Identify the blood parasite species.
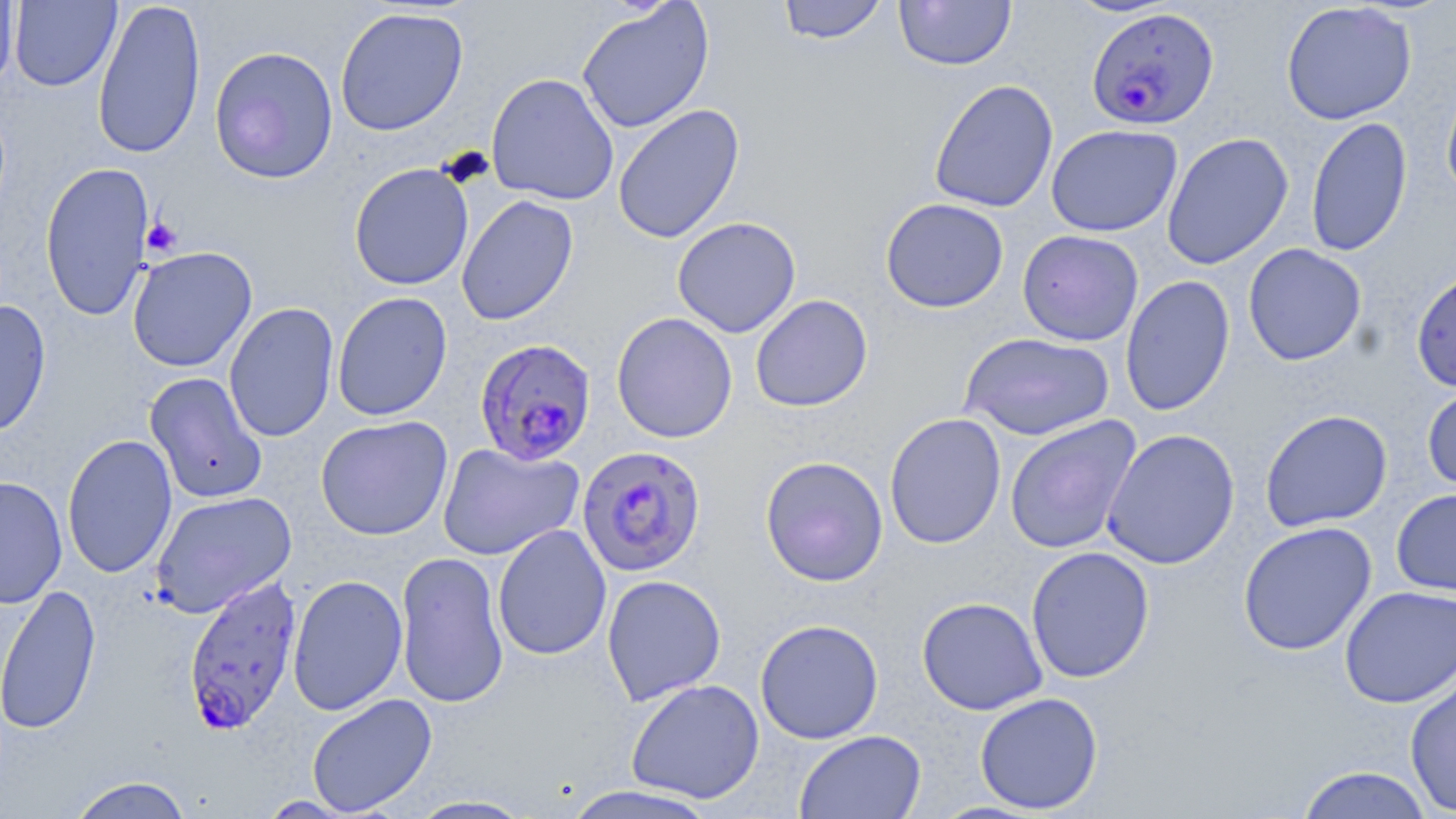

Plasmodium falciparum.

Summary:
  - Coordinate format: approximate bounding boxes as [x1, y1, x2, y2] in pixels
  - Uninfected red blood cell locations: [0, 0, 19, 94], [92, 0, 206, 160], [777, 0, 888, 45], [894, 0, 1016, 71], [1063, 0, 1181, 17], [9, 1, 122, 91], [1281, 1, 1417, 125], [576, 2, 714, 134], [334, 7, 469, 136], [209, 46, 339, 184], [486, 72, 619, 205], [1441, 77, 1456, 203], [929, 79, 1059, 213], [613, 103, 745, 244], [1306, 116, 1412, 257], [1046, 124, 1182, 236], [1161, 132, 1294, 270], [40, 160, 155, 322], [349, 162, 474, 291], [456, 195, 579, 326], [880, 197, 1009, 313], [672, 216, 801, 338], [1017, 229, 1143, 346], [1243, 243, 1367, 366], [127, 247, 257, 372], [1411, 268, 1456, 392], [1120, 274, 1235, 416], [332, 291, 452, 421], [750, 295, 873, 412], [0, 299, 51, 437], [224, 302, 340, 443], [611, 312, 738, 443], [960, 332, 1115, 440], [144, 372, 267, 503], [1422, 382, 1456, 494], [1260, 409, 1393, 532], [884, 413, 1007, 549], [315, 415, 453, 541], [1004, 415, 1142, 555], [1101, 428, 1240, 570], [62, 433, 177, 578], [438, 442, 584, 560], [760, 456, 888, 586], [0, 475, 68, 608], [1391, 488, 1456, 598], [150, 491, 298, 618], [1237, 521, 1377, 656], [493, 524, 612, 661], [1025, 546, 1154, 684], [395, 550, 509, 710], [287, 574, 408, 715], [601, 574, 726, 706], [0, 583, 102, 735], [1339, 586, 1456, 708], [916, 596, 1048, 715], [755, 619, 884, 745], [1404, 669, 1456, 817], [626, 678, 765, 803], [974, 692, 1104, 814], [306, 693, 437, 816], [794, 729, 926, 819], [1296, 766, 1435, 818], [67, 775, 194, 819], [559, 785, 722, 818], [406, 795, 536, 818], [257, 796, 358, 818]
  - Plasmodium falciparum-infected red blood cell locations: [1086, 7, 1219, 132], [474, 337, 597, 466], [577, 444, 706, 576], [182, 576, 303, 735]
  - Platelet locations: [141, 217, 183, 258]
  - Field of view: one of a larger specimen
  - Modality: light microscopy
  - Preparation: thin blood film
  - Image size: 1456×819 pixels
  - Stain: May-Grünwald-Giemsa
  - Magnification: 1000x